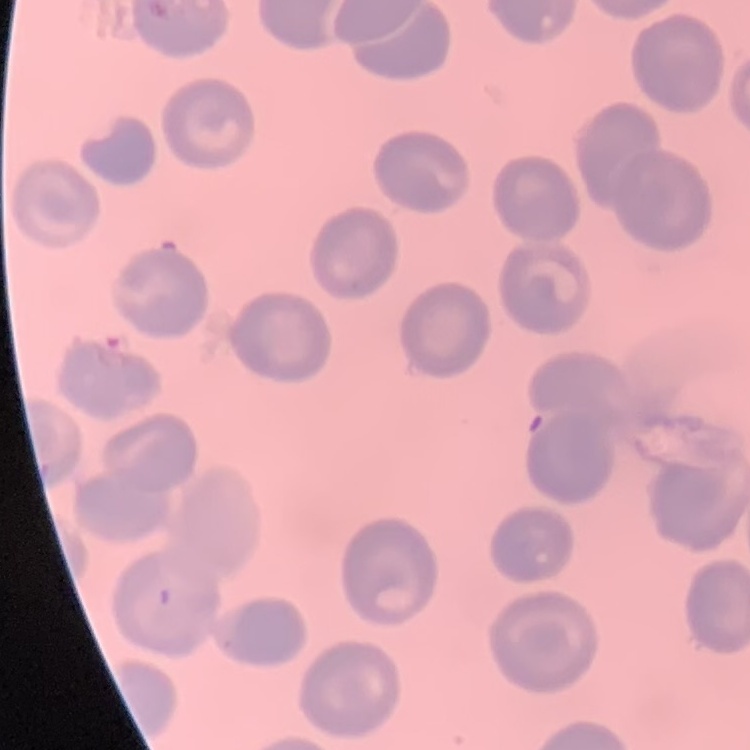
Summary:
  - Erythrocyte morphology: no rouleaux formation
  - Preparation: thin blood smear
  - Image type: one tile cut from a larger photomicrograph
  - Stain: Field's or Giemsa